Assess for malaria.
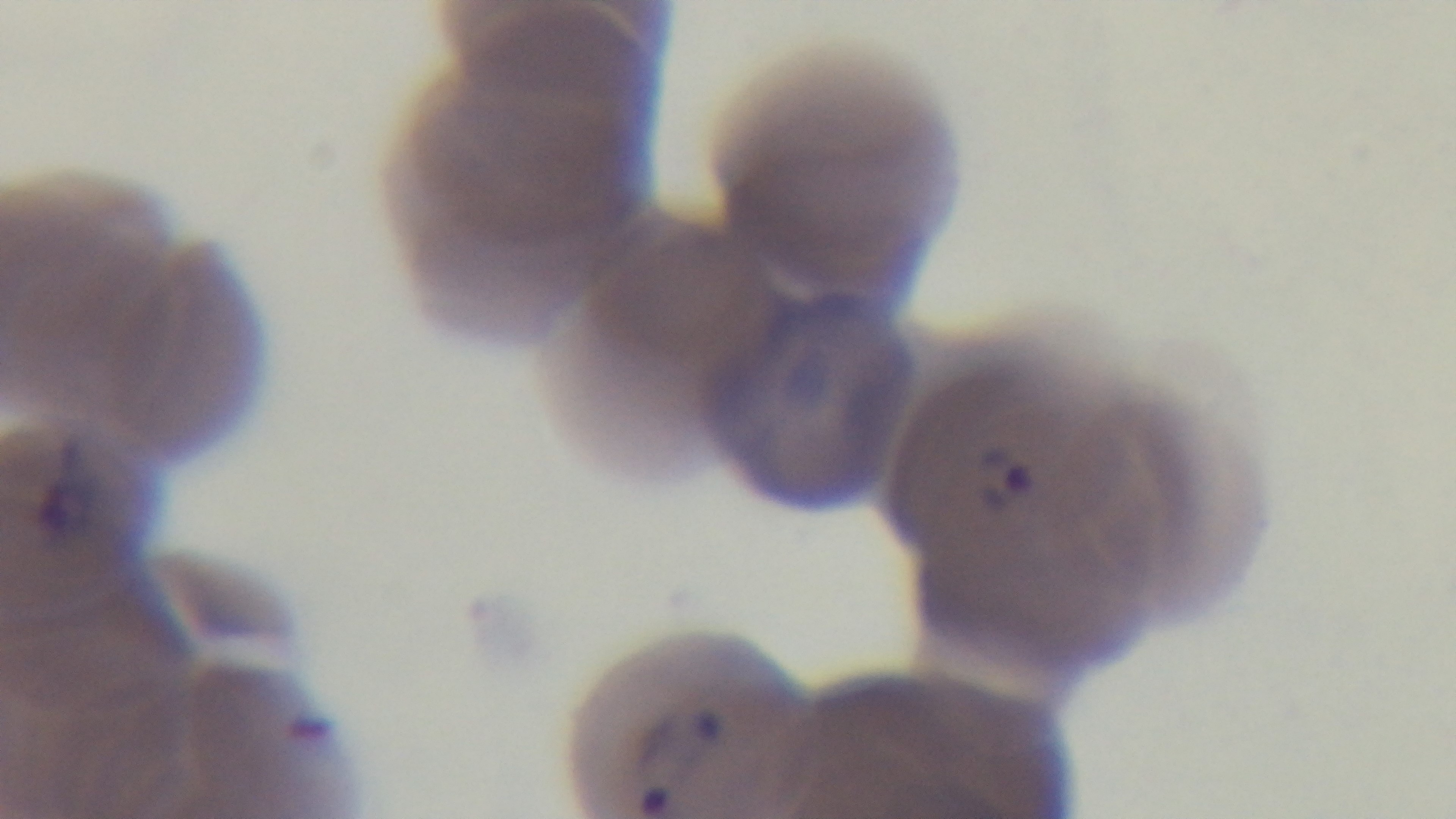
It is infected.

preparation = thin smear
stain = Giemsa
field of view = single
capture = mounted 4K digital camera
modality = light microscopy
objective = 100x oil immersion